Classify this cell by malaria status.
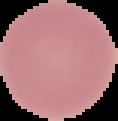
It is uninfected.

Summary:
  - Image type: segmented cell region with the area outside set to black
  - Image size: 118×121 pixels
  - Preparation: thin blood smear